Assess this cell for malaria.
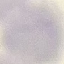

Uninfected.

Summary:
  - Image type: automatically extracted cell patch, resized to 64 × 64 pixels
  - Stain: Giemsa
  - Preparation: thin blood film
  - Capture: smartphone through the microscope eyepiece